Identify the parasite.
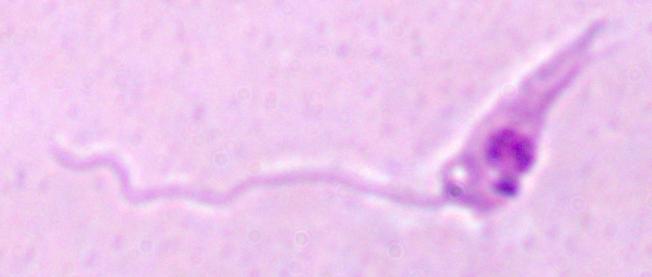

Leishmania.

1000x magnification. Micrograph.